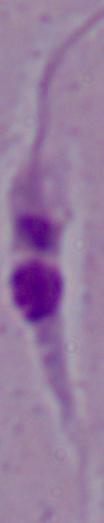
modality = photomicrograph
identification = Leishmania
magnification = 1000x